State the preparation type.
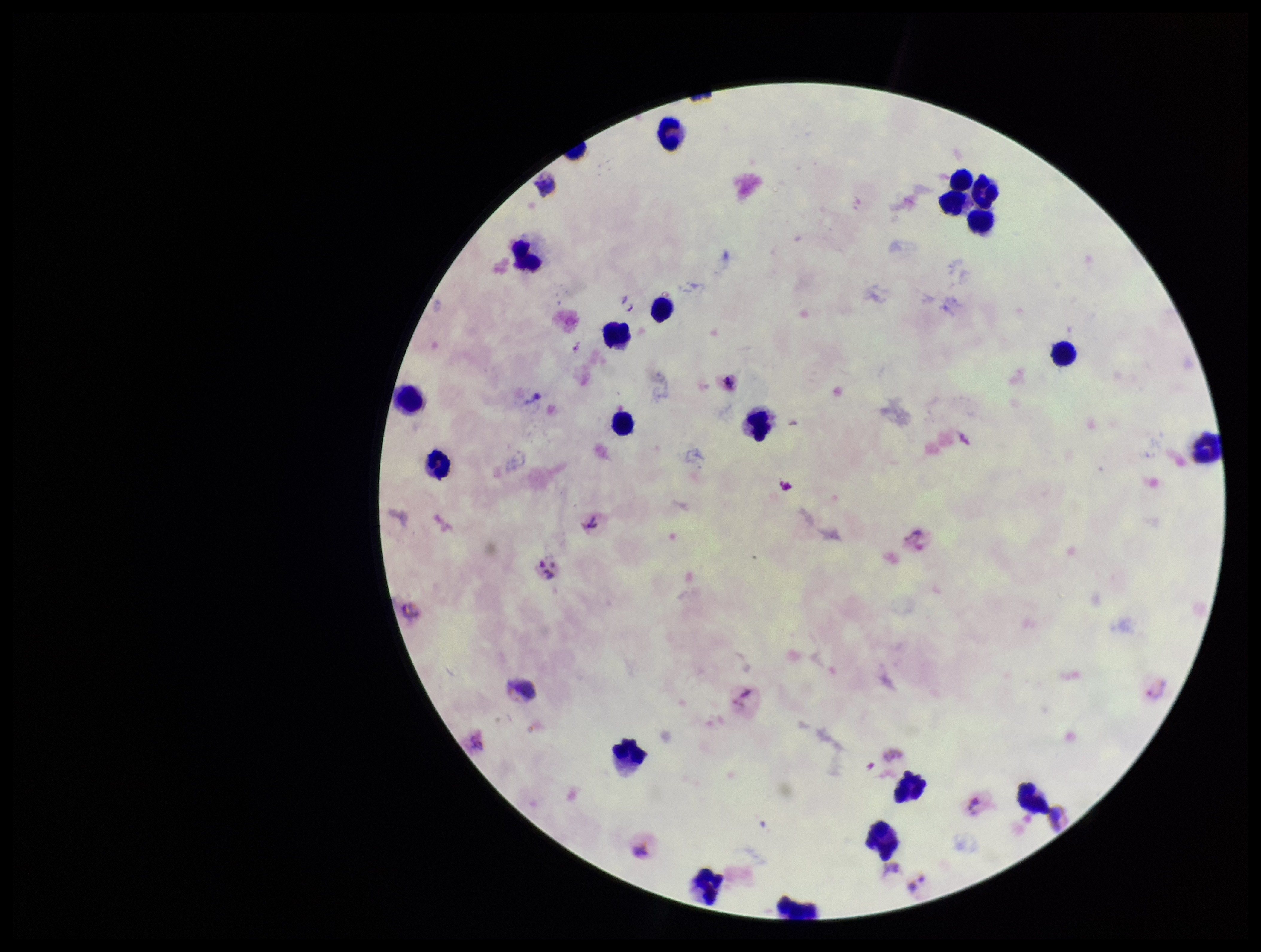
Thick.

Summary:
  - Parasite count: 0
  - Leukocyte count: 21
  - Stain: Giemsa
  - Patient malaria status: positive
  - Image size: 1261×952 pixels
  - Capture: smartphone photograph through the microscope eyepiece
  - Plasmodium parasites: none detected
  - Field of view: single
  - Species reported for this patient: Plasmodium vivax